Assess this cell for malaria.
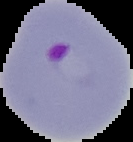

Parasitized.

image size = 133×142 pixels
image type = cell region segmented out of the field of view; surrounding area masked to black
preparation = thin blood smear